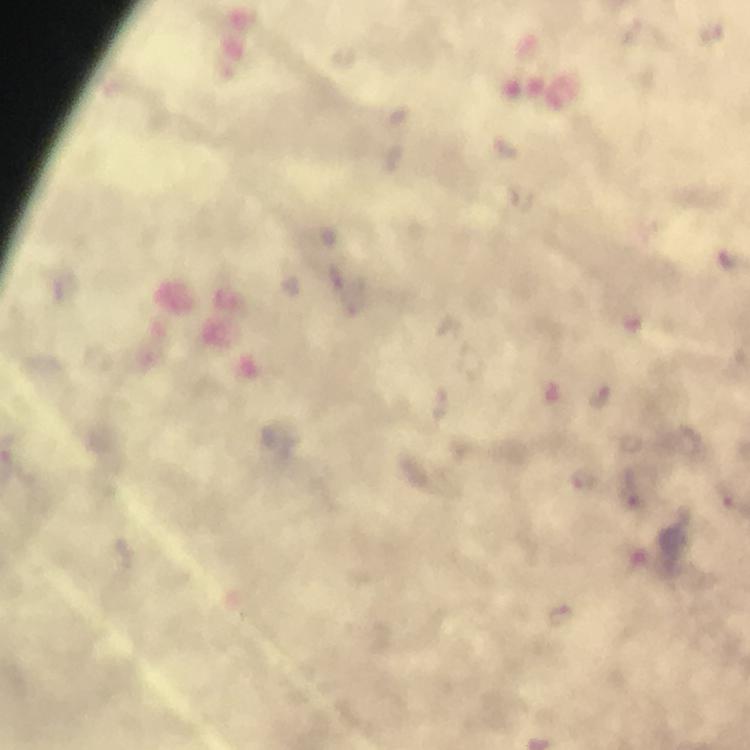

Approximate centers as [x, y] in pixels.
Summary:
  - Plasmodium parasite locations: [730, 258], [601, 396], [583, 479], [641, 489]
  - Preparation: thick smear
  - Stain: Giemsa
  - Capture: smartphone mounted on the microscope
  - Magnification: 100x
  - Immersion oil: applied
  - Image size: 750×750 pixels
  - Cropped from: a single field of view
  - Context: from a diagnostic examination for malaria